Classify this cell by malaria status.
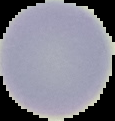
Uninfected.

{
  "image_size": "115×121 pixels",
  "image_type": "cell region segmented out of the field of view; surrounding area masked to black",
  "preparation": "thin blood film"
}